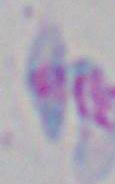

modality = photomicrograph
magnification = 1000x
identification = Toxoplasma gondii